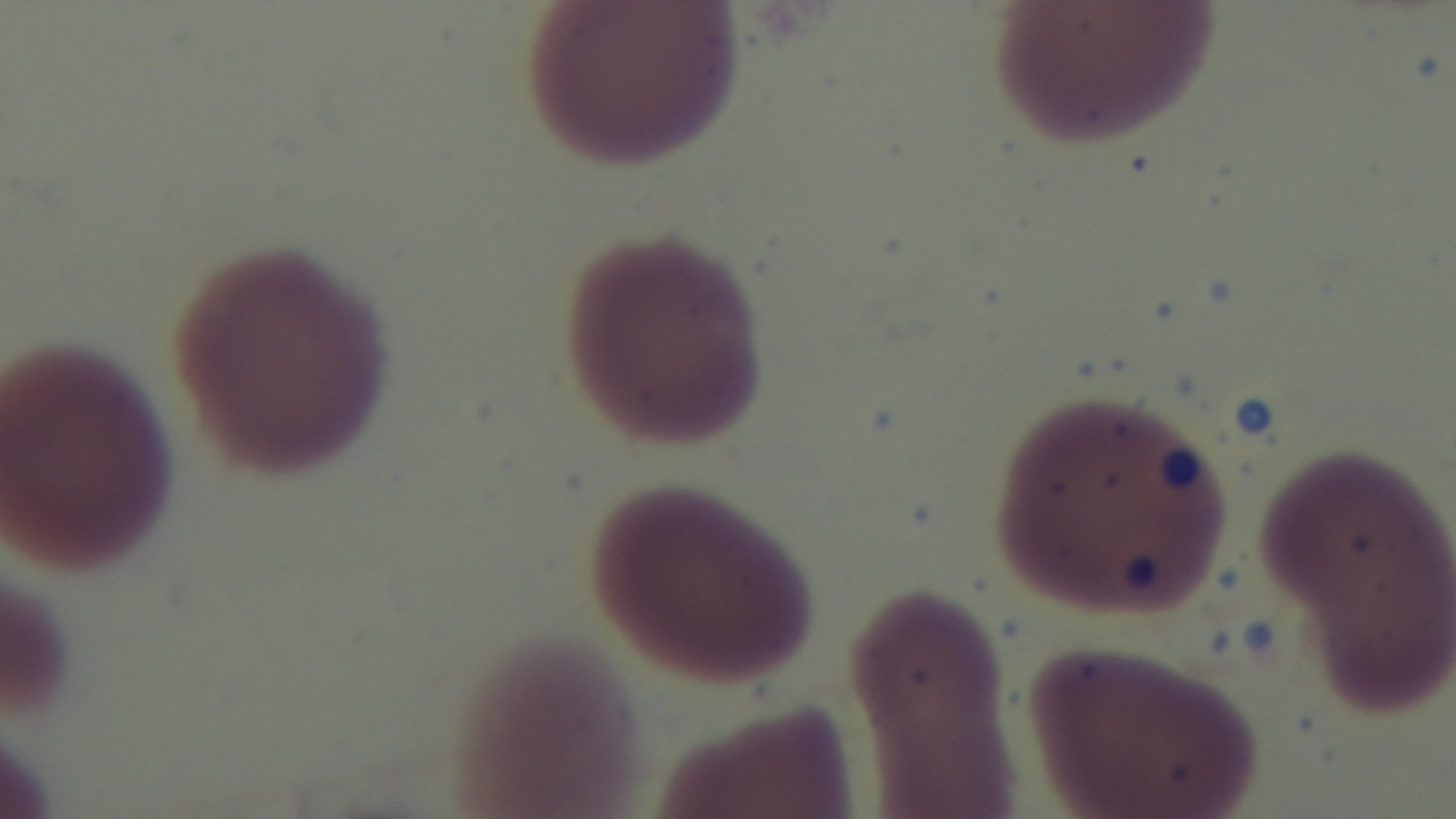
{
  "objective": "100x oil immersion",
  "modality": "light microscopy",
  "malaria_status": "uninfected",
  "field_of_view": "single",
  "stain": "Giemsa",
  "capture": "mounted 4K digital camera",
  "preparation": "thin"
}